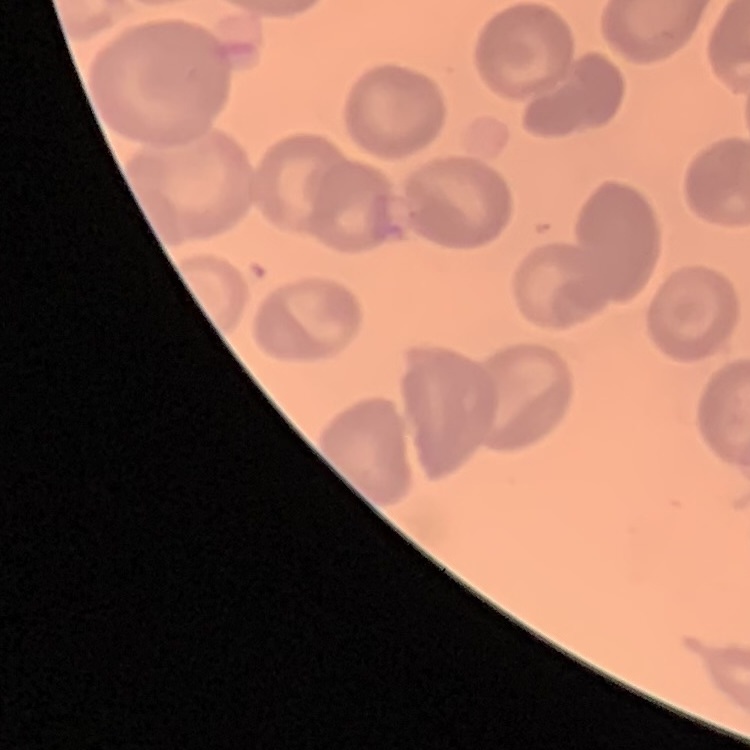 The red blood cells show no rouleaux formation. Stained with either Field's or Giemsa. Thin blood film. One tile cut from a larger photomicrograph.